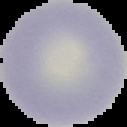
Summary:
  - Image type: cell region segmented out of the field of view; surrounding area masked to black
  - Preparation: thin blood smear
  - Image size: 127×127 pixels
  - Malaria status: uninfected